State which cell type is depicted.
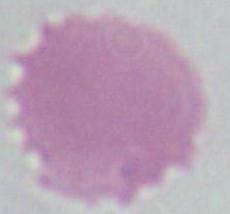

An erythrocyte.

magnification = 1000x
modality = photomicrograph